Comment on the morphology of the red blood cells.
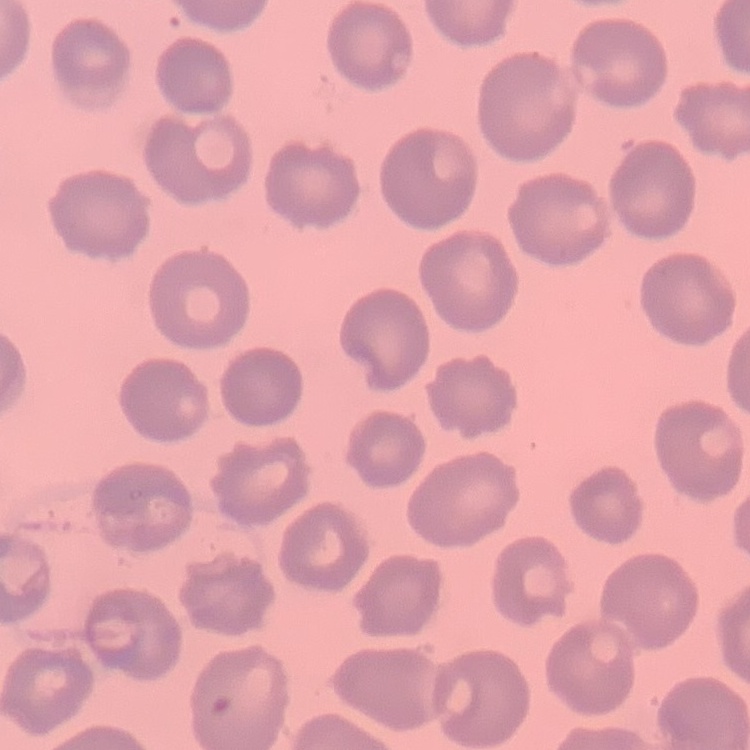

They show no rouleaux formation.

stain = Field's or Giemsa
preparation = thin blood film
image type = one tile cut from a larger photomicrograph